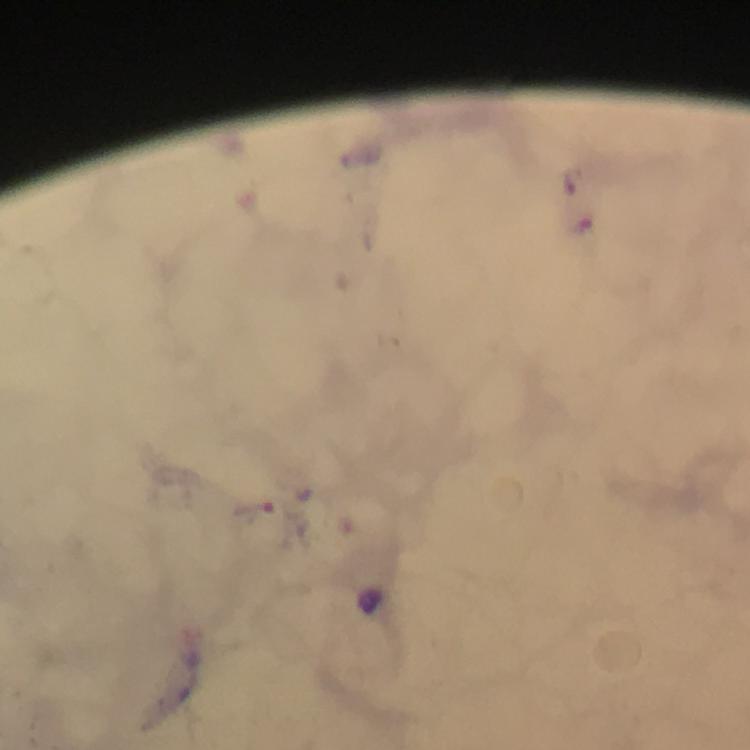

capture = smartphone mounted on the microscope
immersion oil = applied
Plasmodium parasite locations = approximate object centers, in pixels from the top-left corner: (x=255, y=509)
cropped from = a single field of view
magnification = 100x
context = from a diagnostic examination for malaria
preparation = thick blood smear
stain = Giemsa
image size = 750×750 pixels